Assess this cell for malaria.
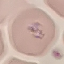
Uninfected.

Summary:
  - Capture: smartphone through the microscope eyepiece
  - Stain: Giemsa
  - Preparation: thin blood film
  - Image type: automatically extracted cell patch, resized to 64 × 64 pixels